Name the parasite shown.
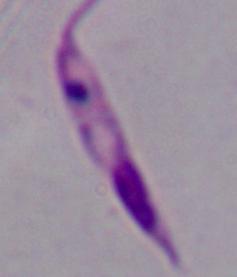

Leishmania.

Captured at 1000x magnification. Micrograph.